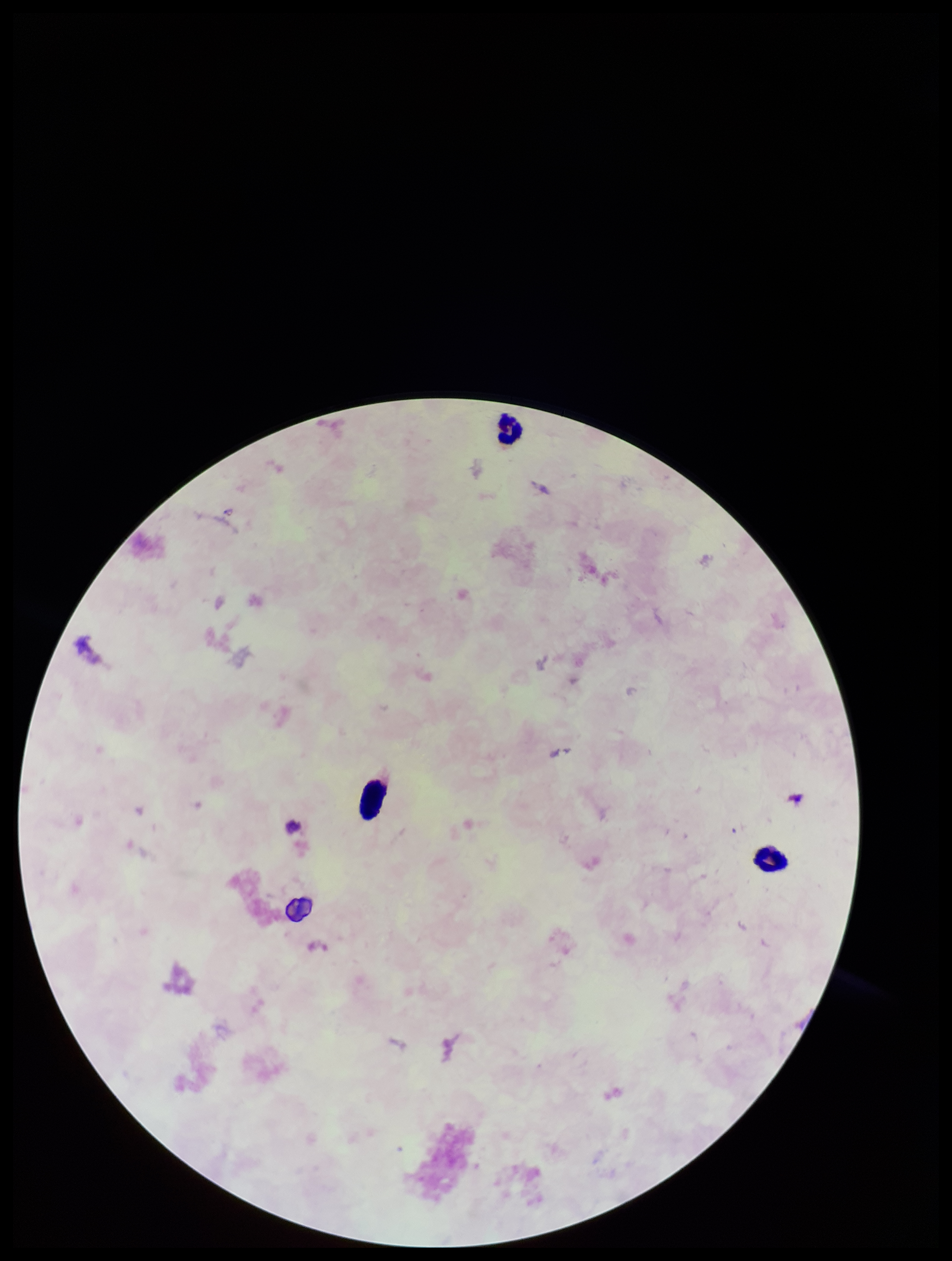 Single field of view. Preparation: thick smear. Image is 952×1261 pixels. Parasite count: 0. Leukocyte count: 3. Stained with Giemsa. Patient malaria status: negative. Smartphone photograph taken through the eyepiece of a microscope. Plasmodium parasites: none identified.